Assess this cell for malaria.
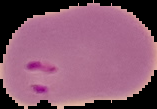

It is parasitized.

Summary:
  - Preparation: thin blood smear
  - Image size: 157×109 pixels
  - Image type: segmented cell region with the area outside set to black